Assess this cell for malaria.
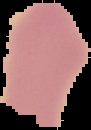

It is uninfected.

image size = 91×130 pixels
preparation = thin blood film
image type = cell region segmented out of the field of view; surrounding area masked to black